Locate every Plasmodium parasite.
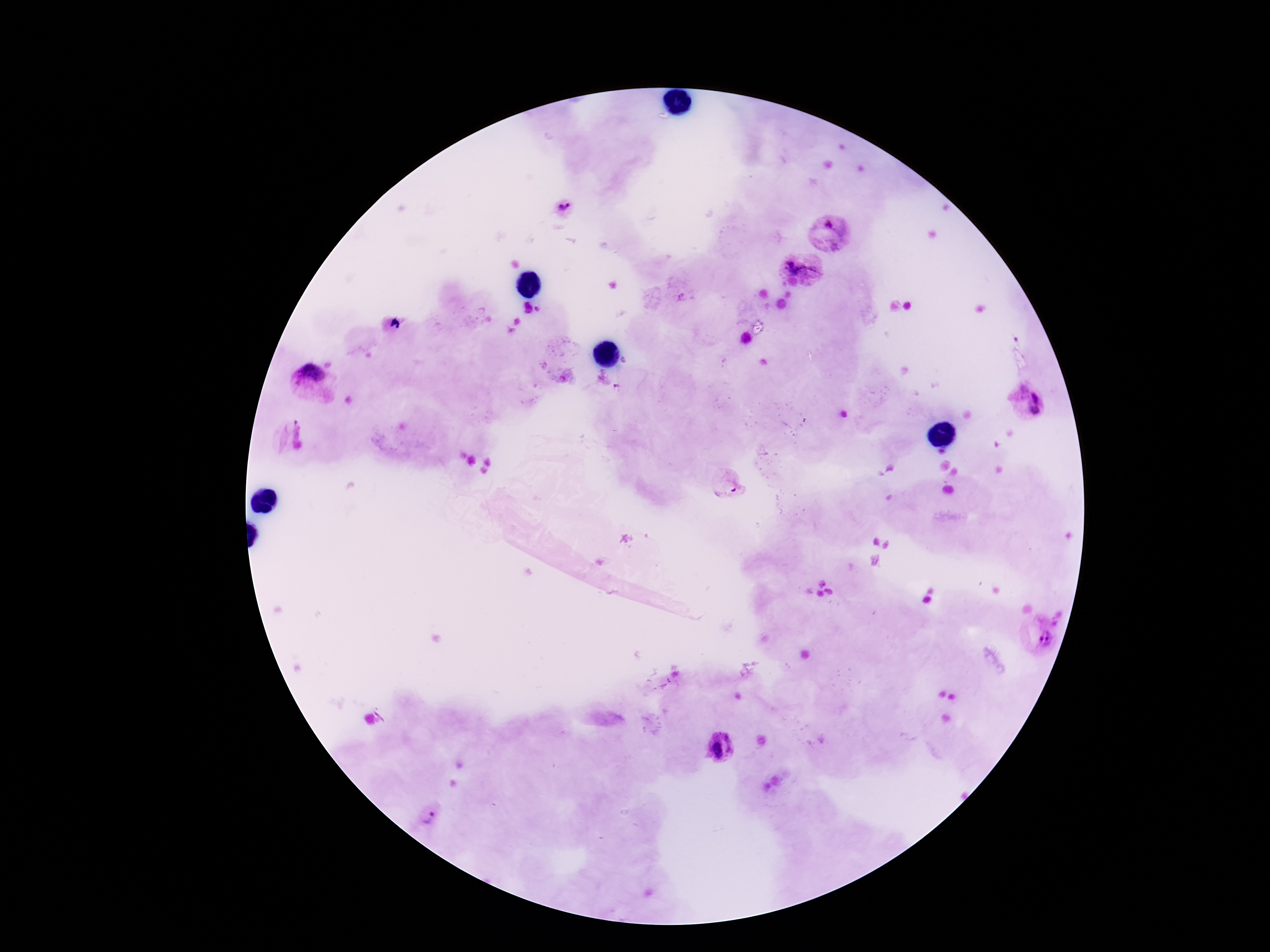
Approximate centers as (x, y) in pixels.
Plasmodium parasites: (565, 208), (830, 234), (801, 271), (308, 383), (1034, 394), (1035, 412), (292, 437), (729, 487), (1039, 639), (721, 747), (430, 817).

Summary:
  - Field of view: single
  - Preparation: thick blood film
  - Patient malaria status: infected
  - Image size: 1270×952 pixels
  - Capture: smartphone camera through the microscope eyepiece
  - Magnification: 100x
  - Stain: Giemsa